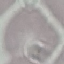
Malaria status: uninfected. Photographed with a smartphone camera at the microscope eyepiece. Automatically extracted cell patch, resized to 64 × 64 pixels. Thin blood smear. Giemsa-stained preparation.